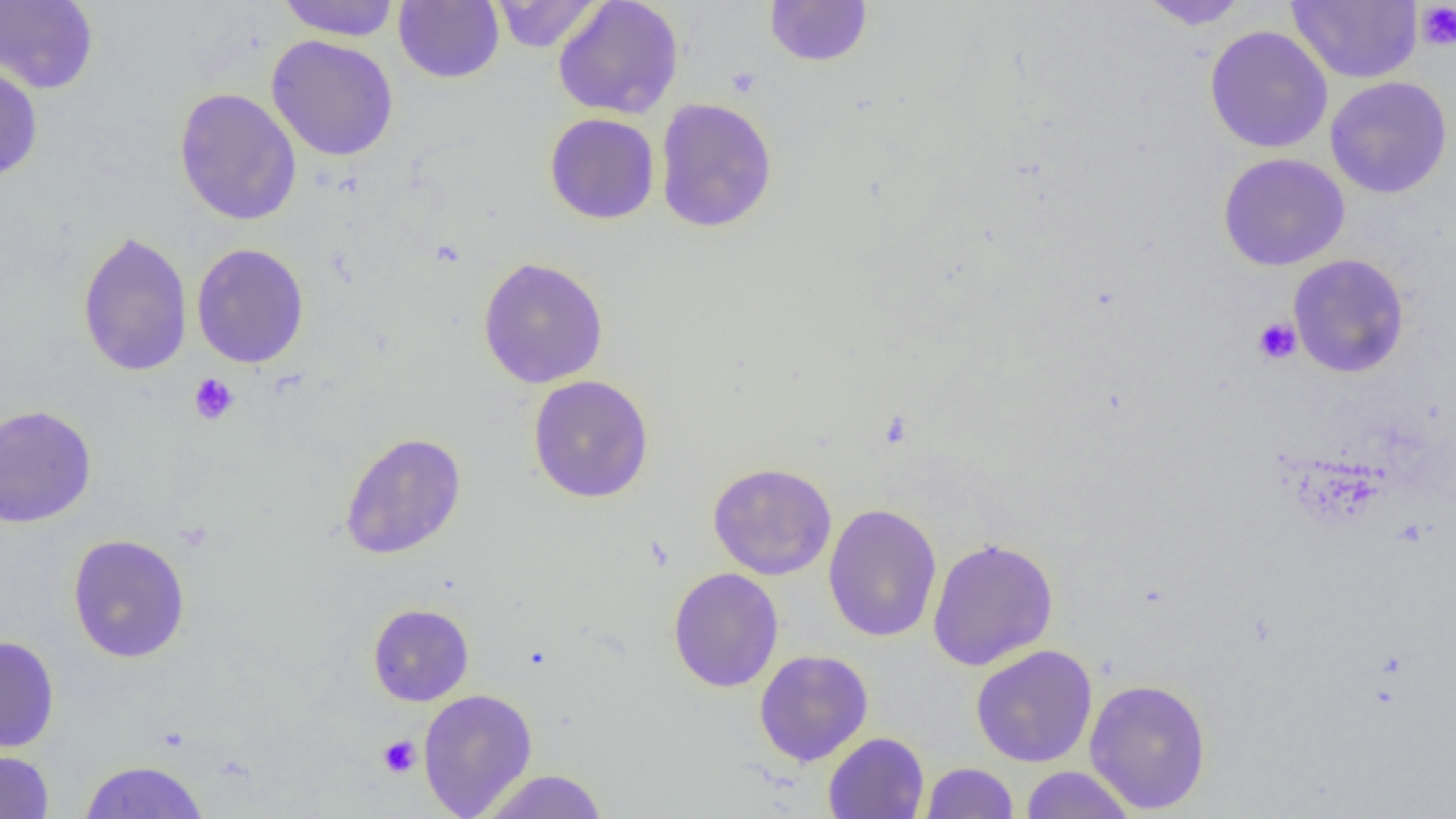
Approximate bounding boxes as [x1, y1, x2, y2] in pixels. Uninfected red blood cell locations: [276, 0, 401, 41], [489, 0, 604, 53], [552, 0, 684, 120], [764, 0, 873, 67], [1138, 0, 1252, 29], [1287, 0, 1423, 84], [0, 1, 99, 93], [394, 1, 504, 84], [1204, 25, 1334, 154], [266, 34, 399, 162], [0, 62, 43, 182], [1325, 76, 1453, 199], [174, 87, 302, 226], [654, 97, 778, 233], [544, 112, 660, 225], [1217, 152, 1350, 271], [77, 231, 193, 376], [191, 243, 309, 368], [1288, 254, 1410, 378], [478, 257, 609, 389], [528, 375, 654, 503], [0, 405, 96, 528], [339, 432, 466, 560], [707, 462, 837, 580], [823, 503, 942, 643], [67, 534, 191, 663], [926, 537, 1059, 671], [668, 567, 784, 693], [368, 603, 474, 706], [0, 635, 60, 753], [970, 644, 1098, 767], [754, 649, 874, 767], [1084, 677, 1212, 814], [418, 688, 537, 818], [823, 732, 929, 819], [0, 746, 55, 818], [78, 760, 210, 819], [920, 762, 1019, 818], [1020, 766, 1136, 818], [476, 769, 610, 818]. Platelet locations: [1415, 2, 1456, 51], [1252, 317, 1302, 365], [188, 373, 239, 425], [378, 735, 421, 778]. Slide-level diagnosis: no evidence of blood parasites. 1000x magnification. Thin blood film. Light microscopy. Image is 1456×819 pixels. One field of a larger specimen.